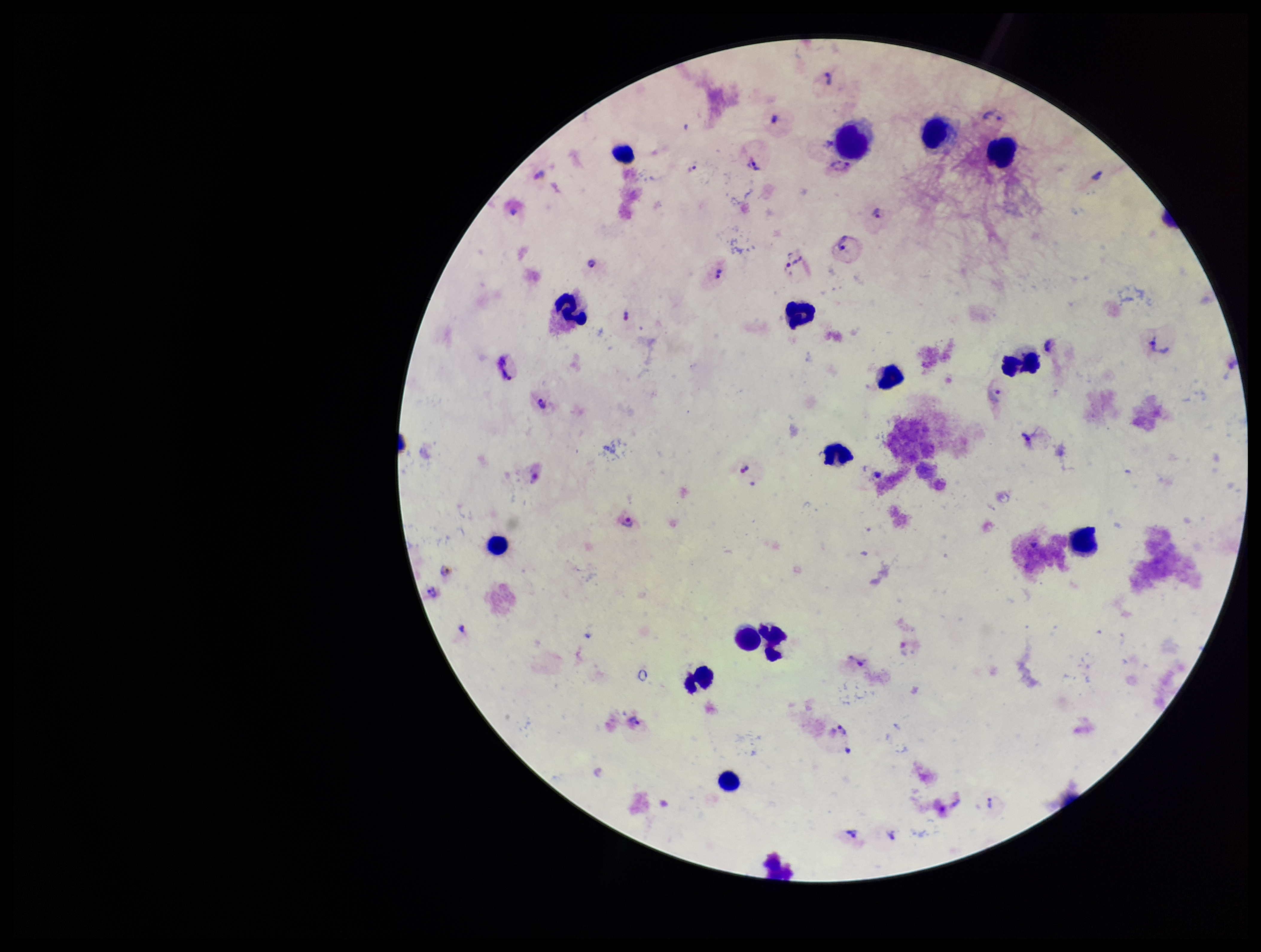
preparation = thick smear
leukocyte count = 15
image size = 1261×952 pixels
Plasmodium parasites = identified
species reported for this patient = Plasmodium vivax
stain = Giemsa
capture = smartphone photograph through the microscope eyepiece
field of view = single
patient malaria status = positive
parasite count = 21